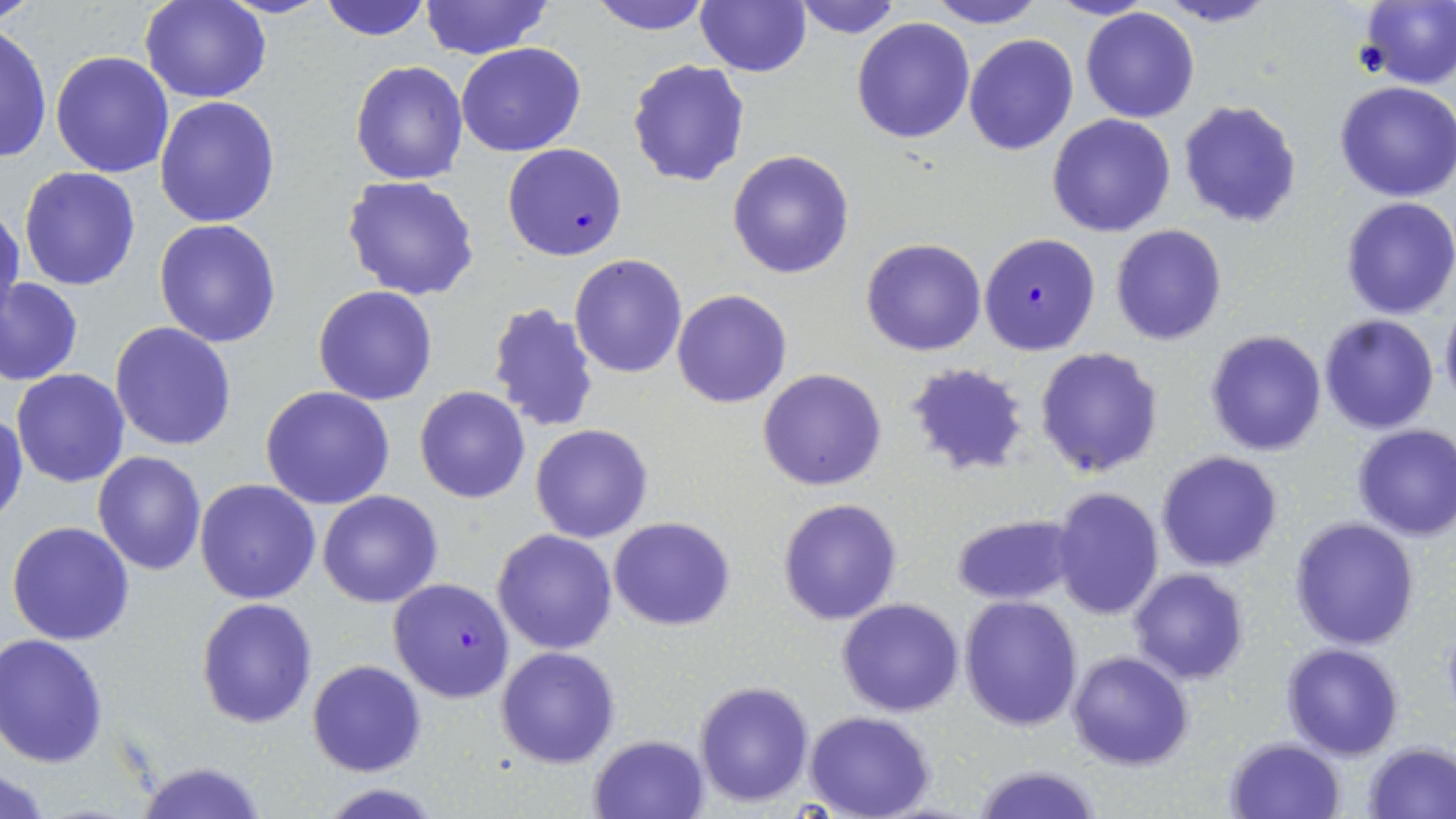

Summary:
  - Coordinate format: approximate bounding boxes as [x1, y1, x2, y2] in pixels
  - Uninfected red blood cell locations: [0, 0, 40, 25], [140, 0, 272, 103], [317, 0, 433, 42], [419, 0, 552, 60], [586, 0, 716, 33], [791, 0, 903, 39], [925, 0, 1046, 28], [1049, 0, 1155, 21], [1156, 0, 1277, 27], [1355, 0, 1456, 87], [695, 1, 811, 76], [1080, 8, 1201, 124], [849, 16, 976, 145], [1, 23, 50, 165], [964, 34, 1079, 156], [455, 42, 586, 157], [50, 49, 175, 178], [627, 59, 750, 187], [350, 61, 469, 185], [1335, 82, 1456, 202], [154, 95, 281, 228], [1177, 99, 1303, 229], [1046, 113, 1176, 237], [727, 150, 855, 278], [18, 167, 142, 291], [342, 175, 480, 300], [1340, 198, 1456, 319], [0, 201, 24, 328], [153, 219, 282, 347], [1110, 224, 1226, 346], [861, 238, 986, 355], [569, 254, 687, 377], [2, 279, 83, 385], [313, 285, 438, 405], [672, 289, 792, 408], [486, 300, 600, 433], [1438, 300, 1456, 410], [1318, 314, 1440, 434], [110, 323, 237, 450], [1205, 329, 1328, 457], [1034, 347, 1163, 479], [905, 361, 1029, 475], [757, 368, 887, 492], [11, 369, 129, 488], [260, 385, 395, 509], [414, 385, 532, 504], [1, 410, 26, 525], [530, 424, 654, 544], [1350, 424, 1456, 540], [93, 450, 207, 576], [1156, 450, 1284, 572], [195, 479, 322, 604], [1050, 488, 1164, 620], [319, 490, 442, 608], [778, 497, 902, 625], [949, 512, 1080, 606], [609, 516, 735, 632], [1290, 517, 1420, 648], [6, 520, 135, 646], [493, 529, 619, 654], [1128, 568, 1248, 684], [959, 596, 1083, 732], [836, 598, 965, 717], [196, 599, 318, 729], [0, 634, 108, 767], [1281, 643, 1404, 759], [496, 646, 620, 767], [1067, 651, 1193, 770], [307, 659, 427, 777], [693, 681, 813, 808], [805, 712, 936, 819], [588, 734, 710, 819], [1224, 737, 1347, 819], [1364, 742, 1456, 818], [132, 760, 269, 819], [970, 763, 1104, 819], [0, 769, 53, 819]
  - Plasmodium falciparum-infected red blood cell locations: [502, 142, 627, 261], [980, 233, 1101, 355], [386, 577, 515, 703]
  - Slide-level diagnosis: Plasmodium falciparum
  - Modality: light microscopy
  - Magnification: 1000x
  - Image size: 1456×819 pixels
  - Preparation: thin blood smear
  - Stain: May-Grünwald-Giemsa
  - Field of view: single